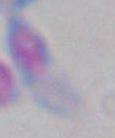

Photomicrograph. Toxoplasma gondii is seen. Captured at 1000x magnification.